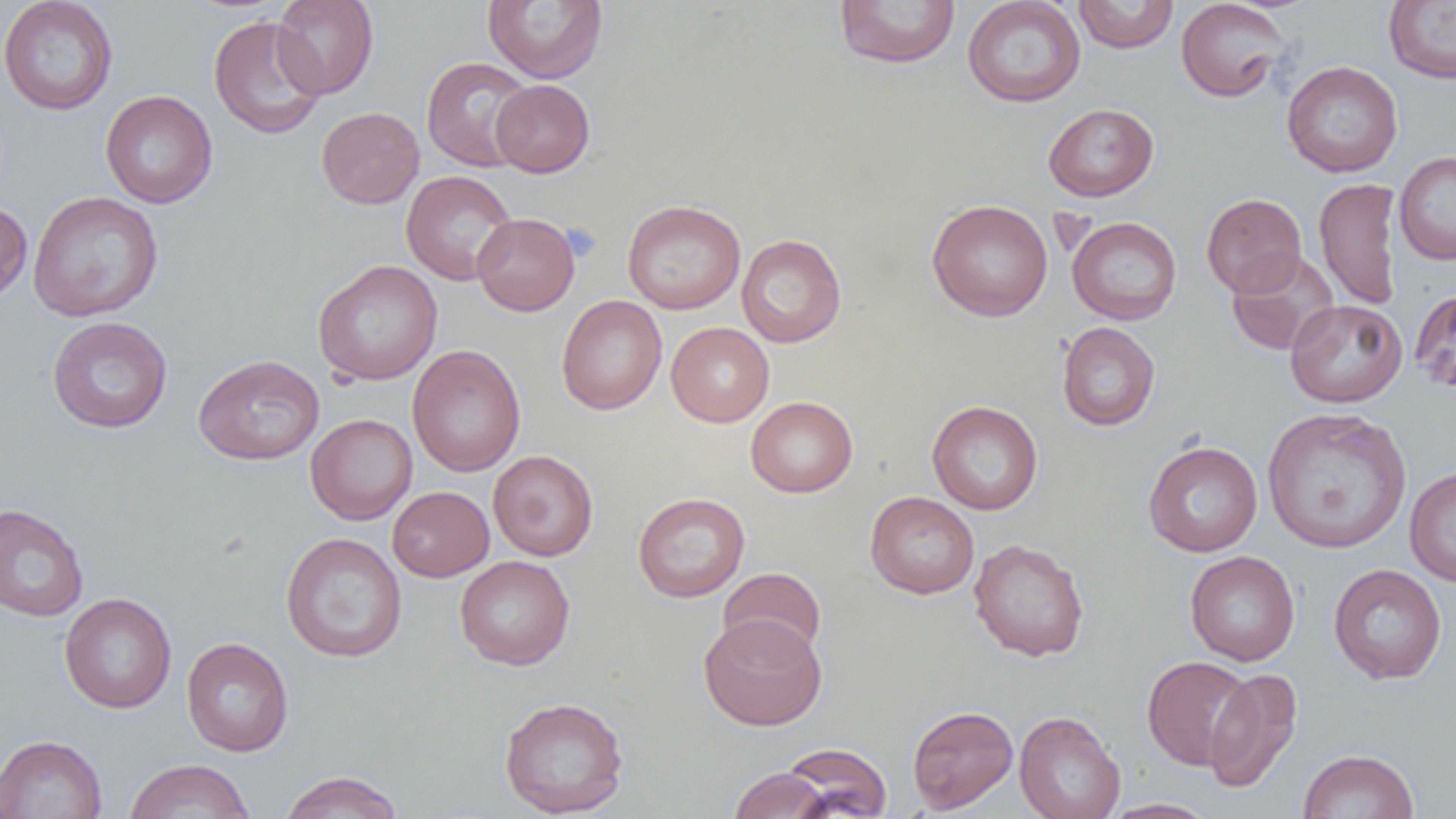

Summary:
  - Coordinate format: approximate bounding boxes as (x1, y1, x2, y2) in pixels
  - Uninfected red blood cell locations: (0, 0, 119, 115), (271, 0, 379, 99), (483, 0, 608, 84), (833, 0, 961, 69), (962, 0, 1086, 107), (1074, 0, 1179, 53), (1383, 0, 1456, 85), (1176, 1, 1290, 102), (208, 16, 327, 140), (421, 56, 536, 172), (1281, 61, 1403, 177), (490, 79, 595, 177), (101, 89, 218, 208), (1043, 103, 1159, 202), (316, 107, 424, 209), (1394, 151, 1456, 264), (401, 170, 518, 285), (1313, 178, 1401, 310), (27, 191, 164, 322), (1201, 193, 1307, 297), (622, 199, 746, 314), (927, 199, 1054, 322), (0, 201, 32, 303), (472, 213, 580, 316), (1067, 216, 1182, 325), (736, 234, 847, 347), (1226, 250, 1340, 356), (313, 260, 443, 385), (1410, 288, 1456, 395), (556, 295, 667, 415), (1285, 299, 1407, 407), (47, 316, 172, 433), (666, 322, 774, 427), (1057, 322, 1160, 431), (407, 344, 525, 477), (193, 354, 324, 465), (745, 396, 858, 497), (927, 400, 1043, 515), (1262, 407, 1412, 554), (305, 413, 418, 525), (1143, 441, 1263, 557), (488, 450, 598, 561), (1404, 466, 1456, 587), (387, 486, 494, 582), (633, 492, 750, 602), (865, 492, 980, 599), (0, 503, 90, 622), (281, 532, 407, 662), (968, 538, 1090, 661), (1185, 551, 1300, 666), (454, 556, 574, 670), (1328, 564, 1447, 685), (718, 567, 827, 660), (59, 593, 176, 714), (699, 613, 827, 730), (181, 637, 294, 756), (1141, 656, 1254, 770), (1204, 667, 1303, 793), (499, 696, 630, 818), (907, 705, 1018, 813), (1014, 711, 1125, 819), (0, 734, 107, 819), (780, 742, 892, 818), (1298, 749, 1418, 819), (122, 759, 255, 819), (728, 767, 833, 819), (278, 770, 404, 819), (1101, 798, 1220, 818)
  - Platelet locations: (561, 223, 601, 261)
  - Slide-level diagnosis: no evidence of blood parasites
  - Field of view: single
  - Modality: optical microscopy
  - Image size: 1456×819 pixels
  - Magnification: 1000x
  - Preparation: thin blood film